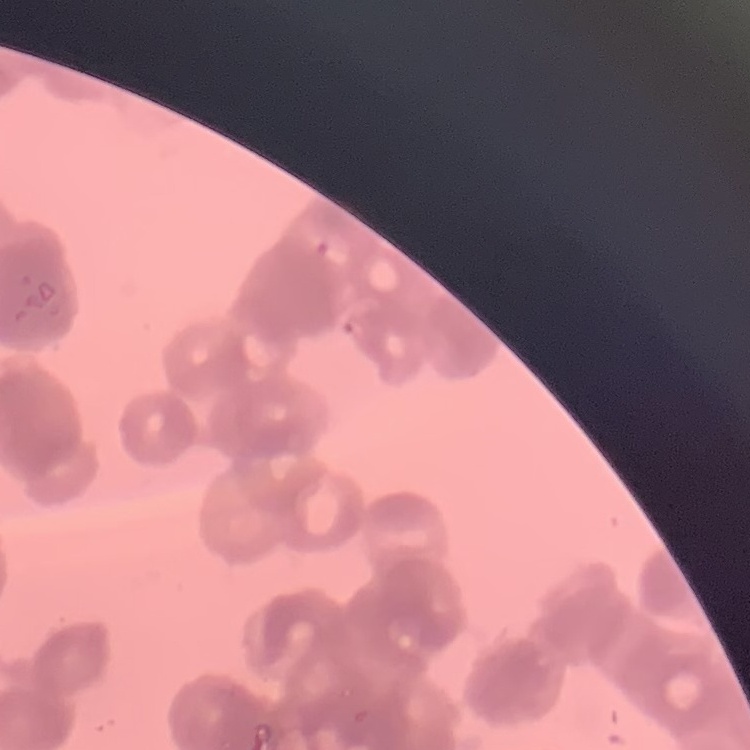

The erythrocytes exhibit rouleaux formation. Field's or Giemsa stain. Square crop of a larger photomicrograph. Thin blood smear.